Assess the morphology of the red blood cells.
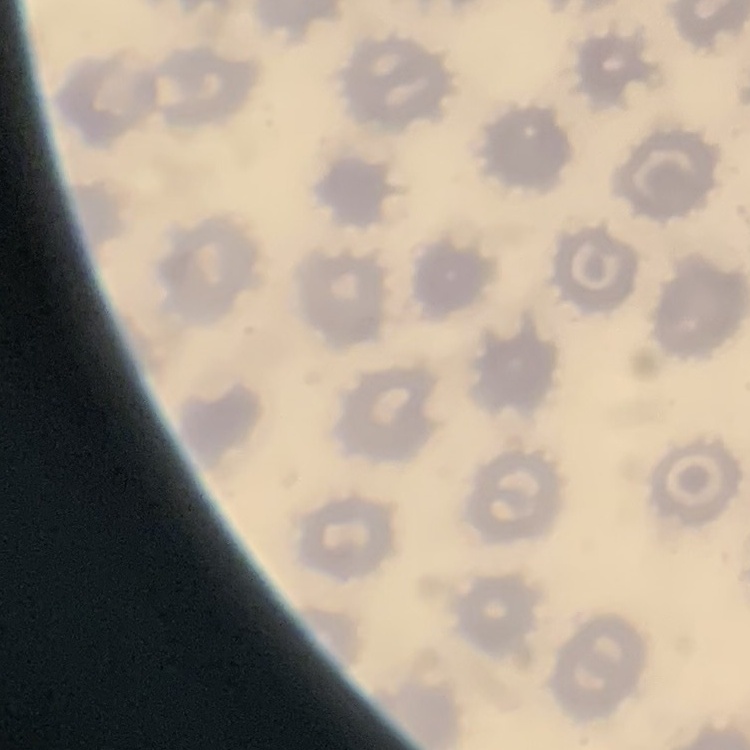
They show no rouleaux formation.

image type = one tile cut from a larger photomicrograph
preparation = thin blood film
stain = Field's or Giemsa